Identify the parasite.
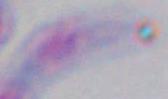
This is Toxoplasma gondii.

Summary:
  - Modality: photomicrograph
  - Magnification: 1000x